Locate and identify every blood parasite.
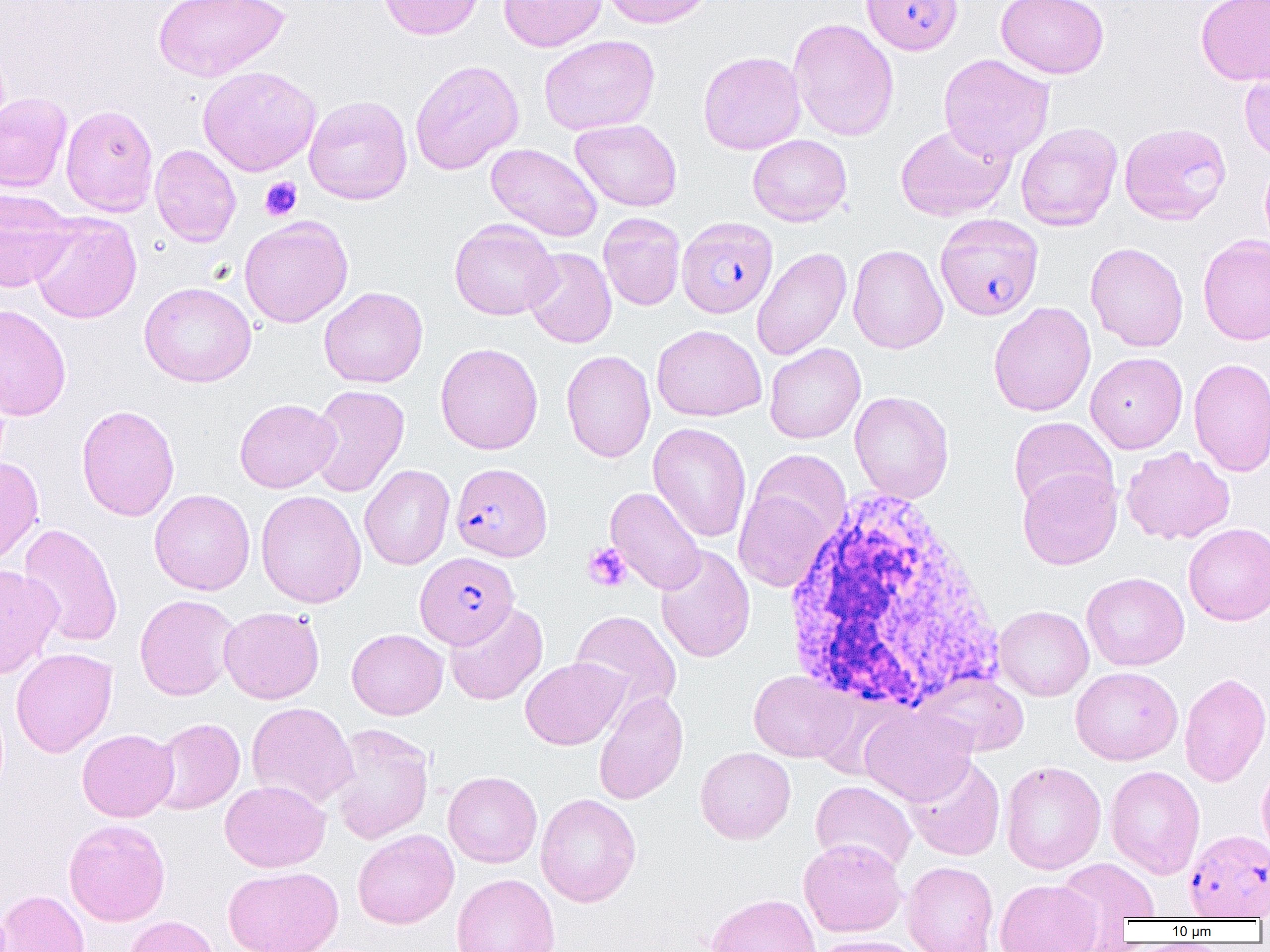

Approximate bounding boxes as (x1, y1, x2, y2) in pixels.
Plasmodium falciparum-infected red blood cells (subset): (861, 0, 963, 55), (935, 213, 1044, 321), (450, 462, 552, 561), (414, 551, 519, 648), (1184, 828, 1270, 920).
No Plasmodium ovale, Plasmodium malariae, Plasmodium vivax, Babesia divergens, or Trypanosoma brucei observed.

slide-level diagnosis = Plasmodium falciparum
field of view = one of a larger specimen
preparation = thin blood film
uninfected red blood cell locations (subset) = approximate bounding boxes as (x1, y1, x2, y2) in pixels: (378, 0, 483, 40), (498, 0, 607, 51), (600, 0, 715, 29), (995, 0, 1109, 79), (1196, 0, 1270, 85), (152, 1, 289, 82), (787, 18, 899, 142), (539, 35, 659, 135), (698, 51, 806, 155), (938, 53, 1054, 163), (410, 59, 524, 175), (1239, 59, 1270, 162), (197, 65, 321, 176), (0, 92, 72, 192), (304, 95, 412, 205), (61, 104, 159, 216), (571, 119, 682, 211), (895, 122, 1015, 221), (1015, 122, 1122, 231), (1119, 122, 1231, 226), (748, 134, 852, 226), (485, 143, 602, 242), (150, 144, 241, 246), (1260, 153, 1270, 255), (0, 189, 79, 293), (30, 213, 141, 324), (598, 213, 685, 311), (239, 215, 353, 327), (449, 218, 560, 320), (1198, 234, 1270, 346), (1085, 242, 1189, 352), (848, 243, 948, 354), (523, 247, 617, 348), (751, 247, 851, 361), (139, 282, 256, 387), (319, 286, 428, 388), (988, 301, 1096, 416), (0, 305, 72, 421), (652, 324, 766, 421), (435, 342, 543, 454), (764, 343, 866, 444), (561, 350, 656, 463), (1085, 352, 1188, 453), (1188, 358, 1270, 477), (307, 384, 410, 498), (849, 391, 954, 503), (234, 398, 340, 493), (76, 404, 180, 521), (1009, 417, 1118, 514), (648, 422, 752, 543), (1121, 447, 1235, 545), (746, 449, 852, 553), (0, 457, 44, 567), (359, 464, 455, 570), (1018, 467, 1122, 570), (606, 486, 706, 595), (733, 487, 835, 593), (149, 489, 255, 595), (256, 490, 366, 608), (18, 523, 123, 648), (1183, 523, 1270, 625), (655, 544, 755, 663), (0, 564, 62, 679), (1082, 572, 1189, 671), (134, 594, 239, 701), (444, 602, 547, 705), (994, 605, 1094, 701), (219, 606, 324, 704), (570, 610, 681, 714), (346, 628, 448, 720), (10, 647, 117, 757), (520, 657, 630, 750), (1070, 666, 1183, 765), (748, 670, 856, 763), (919, 671, 1029, 757), (1179, 672, 1270, 786), (593, 689, 689, 805), (247, 702, 358, 809), (859, 705, 977, 806), (149, 717, 245, 815), (329, 722, 434, 844), (77, 729, 178, 822), (695, 746, 796, 844), (904, 755, 1005, 861), (1257, 760, 1270, 864), (1000, 761, 1106, 874), (1105, 765, 1205, 879), (443, 770, 542, 868), (220, 780, 330, 872), (810, 780, 917, 873), (536, 792, 642, 907), (63, 819, 170, 926), (352, 829, 459, 929), (798, 838, 906, 937), (1054, 857, 1159, 935), (902, 861, 998, 952), (224, 865, 343, 952), (451, 873, 560, 952), (995, 878, 1103, 952), (0, 889, 90, 952), (705, 893, 821, 952), (124, 915, 221, 952), (810, 935, 926, 952)
platelet locations = approximate bounding boxes as (x1, y1, x2, y2) in pixels: (260, 176, 302, 221), (582, 542, 632, 592)
white blood cell locations = approximate bounding boxes as (x1, y1, x2, y2) in pixels: (780, 486, 1003, 718)
modality = optical microscopy
magnification = 1000x
image size = 1270×952 pixels